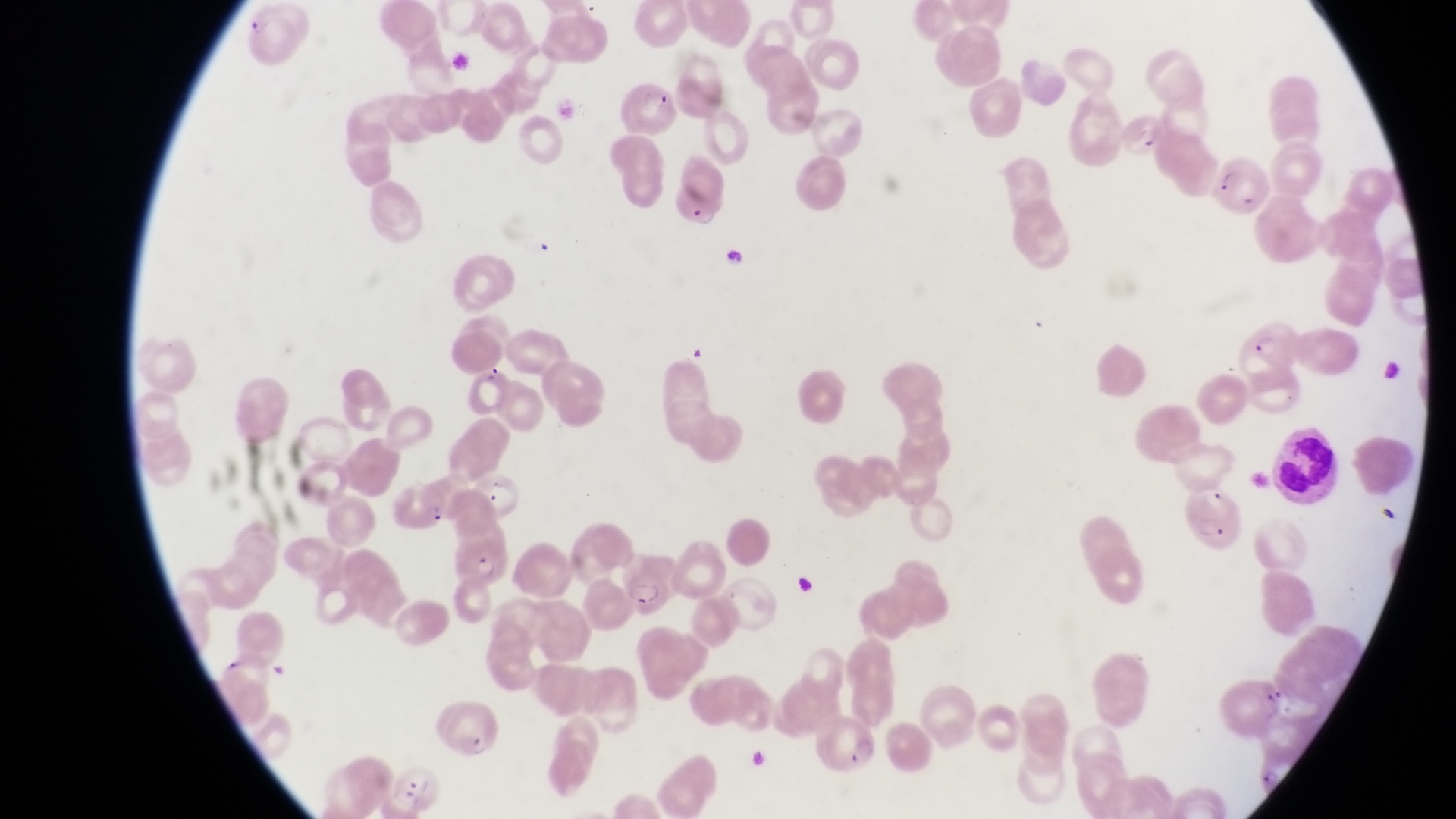
Approximate bounding boxes as left top right bottom in pixels.
Summary:
  - Parasitised red blood cell locations: 620 79 675 137; 1125 108 1167 166; 1213 155 1272 221; 670 158 729 234; 717 238 753 271; 1229 317 1300 383; 466 360 513 421; 391 482 450 534; 455 535 505 587; 613 545 679 621; 439 698 505 764; 380 750 440 813
  - Leukocyte locations: 1268 428 1337 505
  - Preparation: thin blood smear
  - Image size: 1456×819 pixels
  - Country: Uganda
  - Field of view: single
  - Capture: smartphone photograph through the eyepiece of an Olympus CX-23 microscope
  - Magnification: 1000x